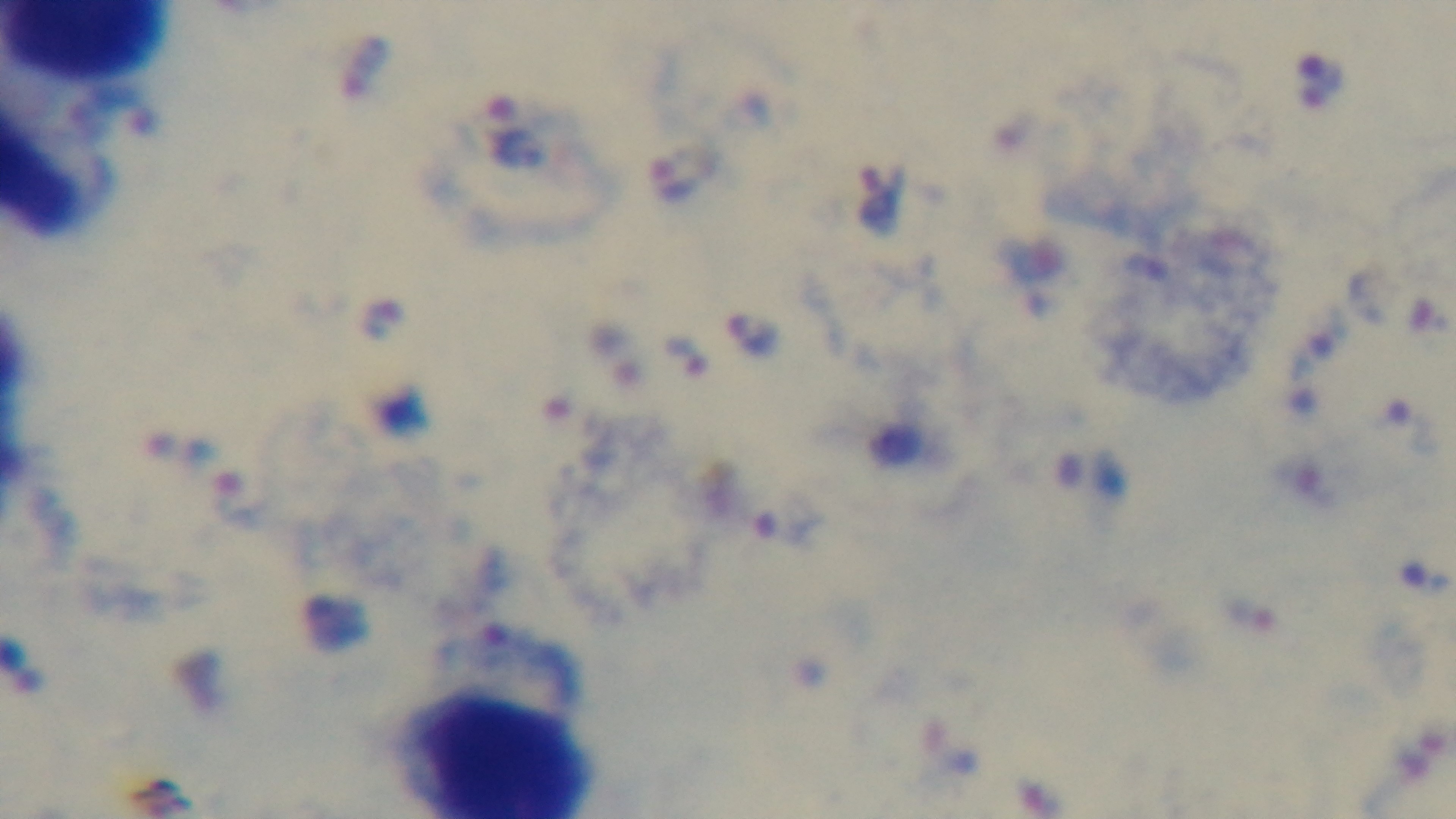
Summary:
  - Malaria status: infected
  - Field of view: one from the slide
  - Modality: light microscopy
  - Preparation: thick blood film
  - Capture: mounted 4K digital camera
  - Stain: Giemsa
  - Objective: 100x oil immersion